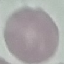

Summary:
  - Malaria status: uninfected
  - Preparation: thin blood smear
  - Stain: Giemsa
  - Capture: smartphone through the microscope eyepiece
  - Image type: cell patch, automatically extracted from a larger field of view and resized to 64 × 64 pixels